Report the malaria status of this cell.
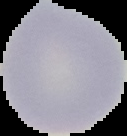
It is uninfected.

Summary:
  - Preparation: thin blood film
  - Image size: 127×136 pixels
  - Image type: cell region segmented out of the field of view; surrounding area masked to black